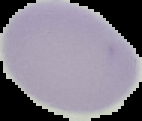
Summary:
  - Preparation: thin blood film
  - Image size: 142×121 pixels
  - Image type: segmented cell region on a black background
  - Malaria status: uninfected